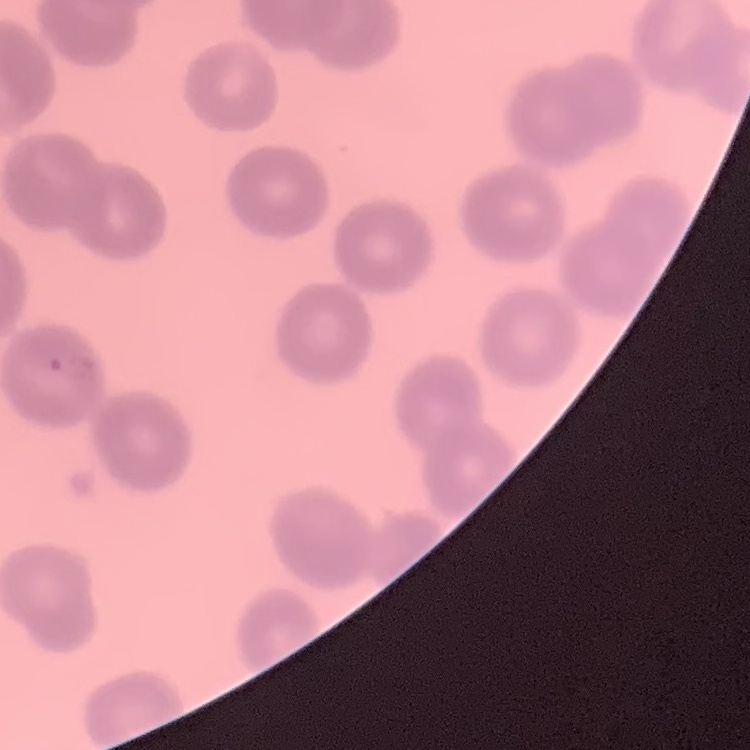

Summary:
  - Erythrocyte morphology: no rouleaux formation
  - Image type: square crop of a larger photomicrograph
  - Stain: Field's or Giemsa
  - Preparation: thin peripheral smear